Comment on the morphology of the erythrocytes.
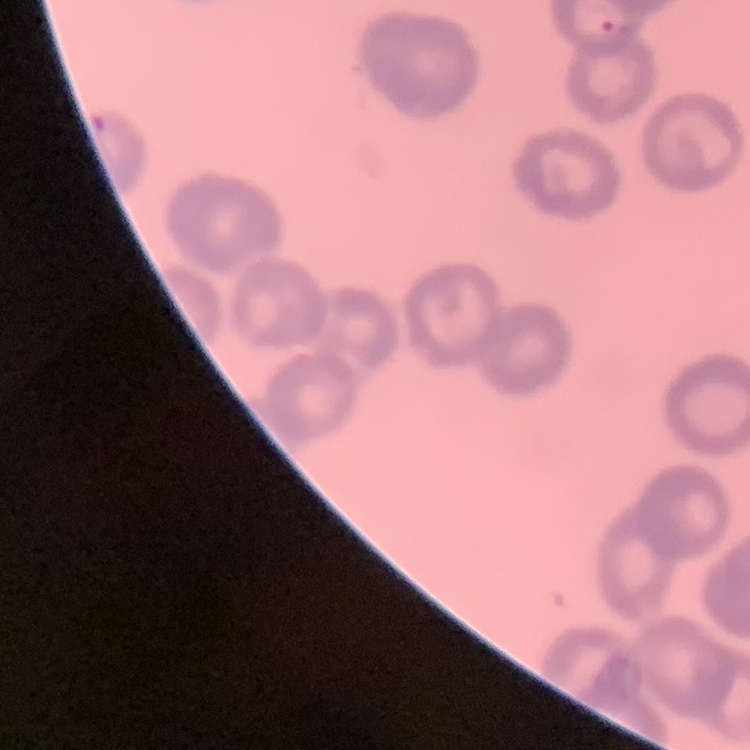
Rouleaux formation.

Summary:
  - Stain: Field's or Giemsa
  - Preparation: thin blood film
  - Image type: square crop of a larger photomicrograph